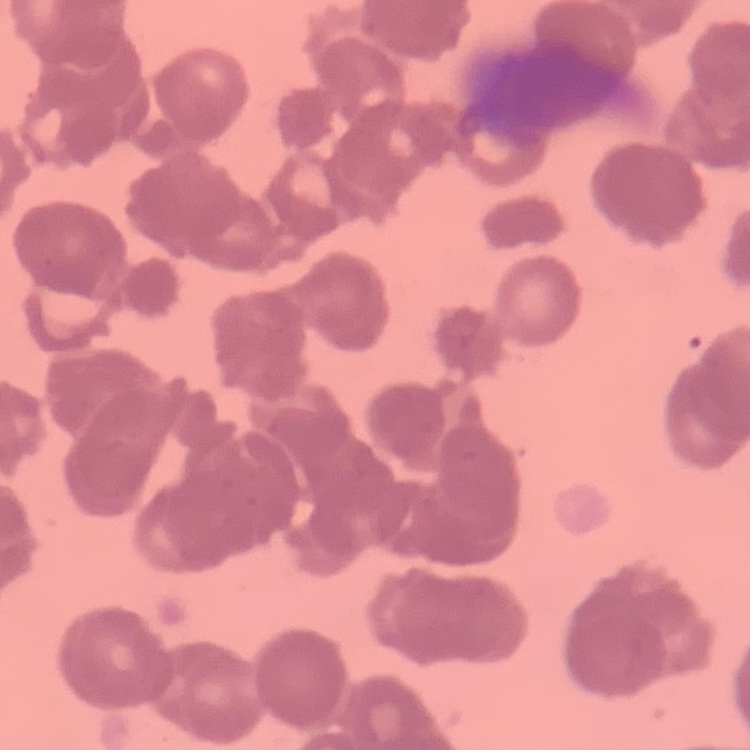
The erythrocytes show rouleaux formation. One tile cut from a larger photomicrograph. Thin peripheral smear. Stained with either Field's or Giemsa.